Assess the morphology of the red blood cells.
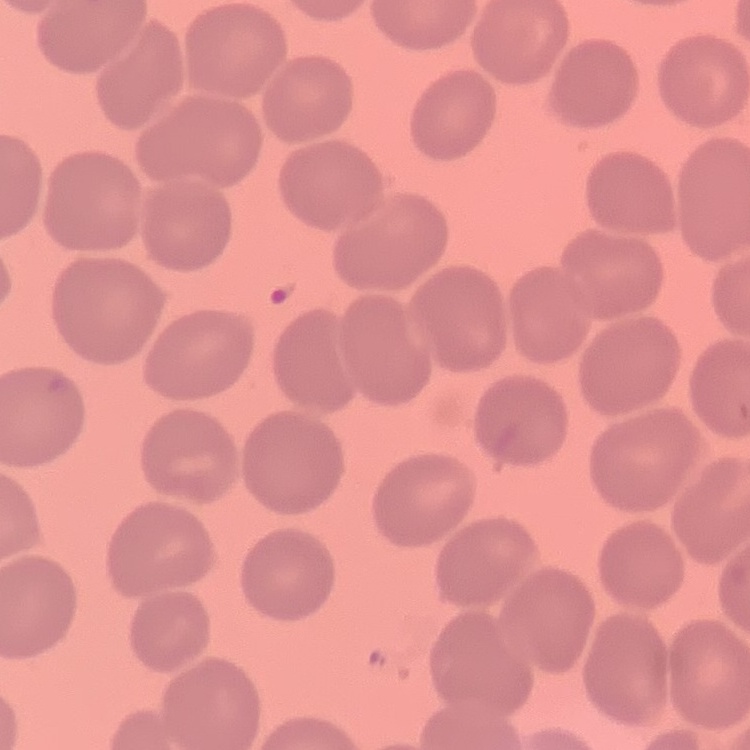
They show no rouleaux formation.

Summary:
  - Preparation: thin blood film
  - Stain: Field's or Giemsa
  - Image type: one tile cut from a larger photomicrograph